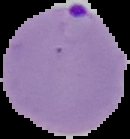

Image is 130×139 pixels. From a thin blood film. Segmented cell region on a black background. Malaria status: parasitized.